Point out each malaria parasite.
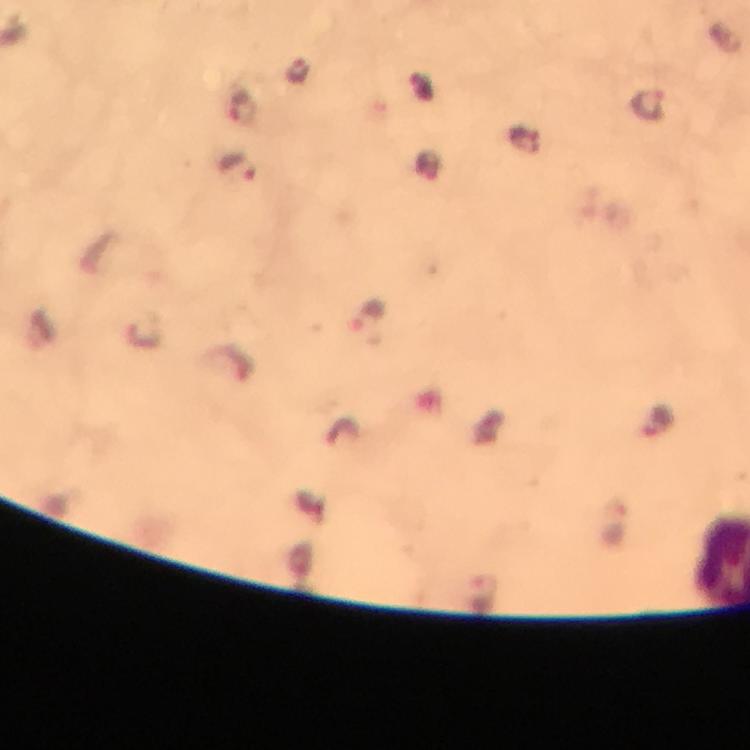

Approximate centers as {x, y} in pixels.
Malaria parasites: {648, 101}, {243, 109}, {236, 166}, {368, 315}, {658, 419}, {479, 590}.

capture = smartphone photograph through a microscope
cropped from = a single field of view
context = from a diagnostic examination for malaria
stain = Giemsa
magnification = 100x
preparation = thick blood film
immersion oil = used
image size = 750×750 pixels